Comment on the morphology of the erythrocytes.
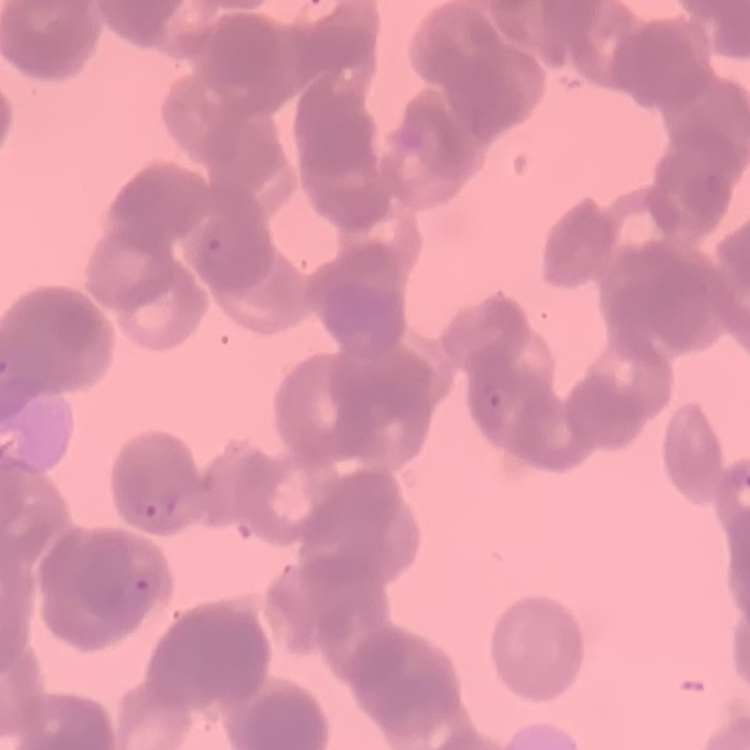
Rouleaux formation.

Stained with either Field's or Giemsa. Thin blood smear. Square crop of a larger photomicrograph.